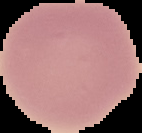 Image is 142×133 pixels. Malaria status: uninfected. The area outside the segmented cell region is set to black. From a thin blood smear.